Assess the morphology of the erythrocytes.
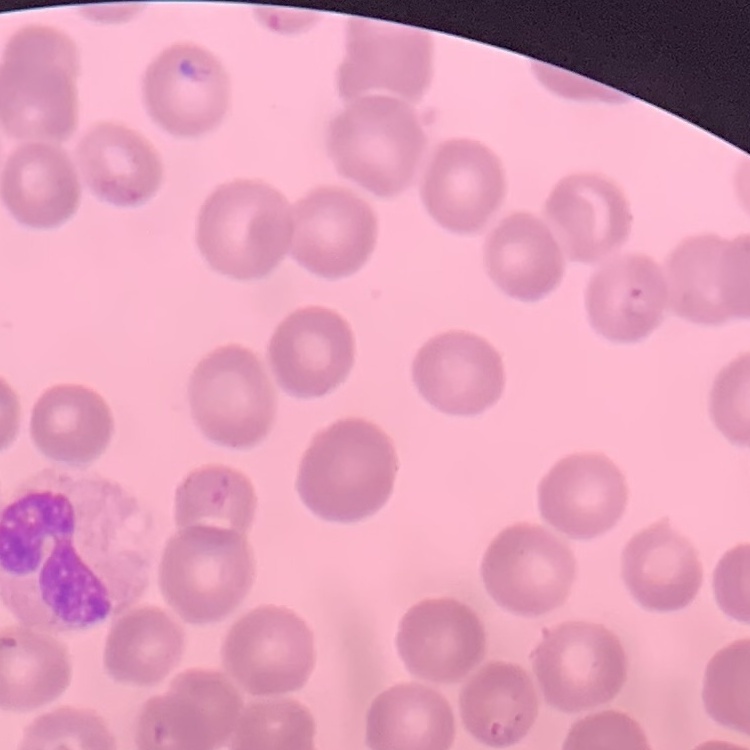
They show no rouleaux formation.

image_type: square crop of a larger photomicrograph
preparation: thin peripheral smear
stain: Field's or Giemsa